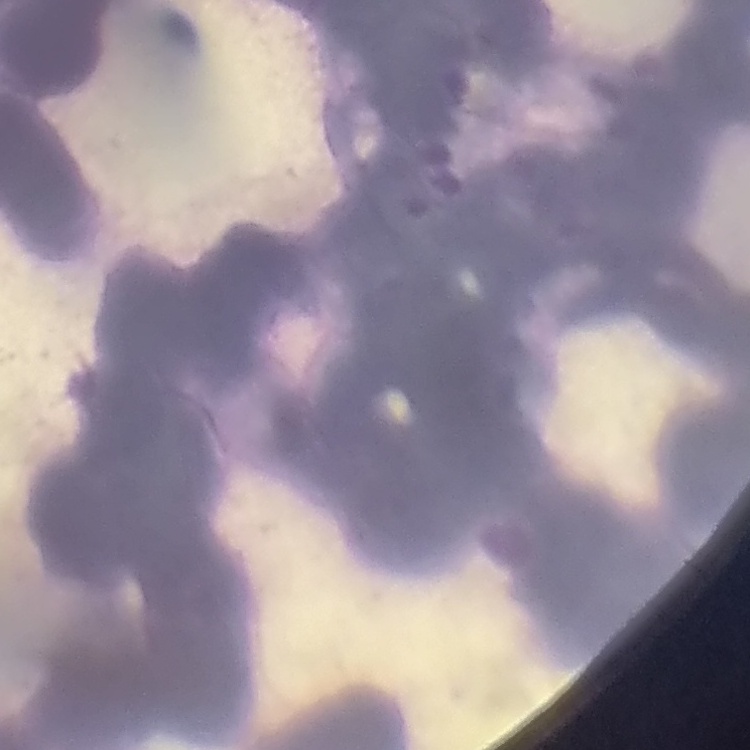
erythrocyte morphology = rouleaux formation
preparation = thin blood film
image type = square crop of a larger photomicrograph
stain = Field's or Giemsa